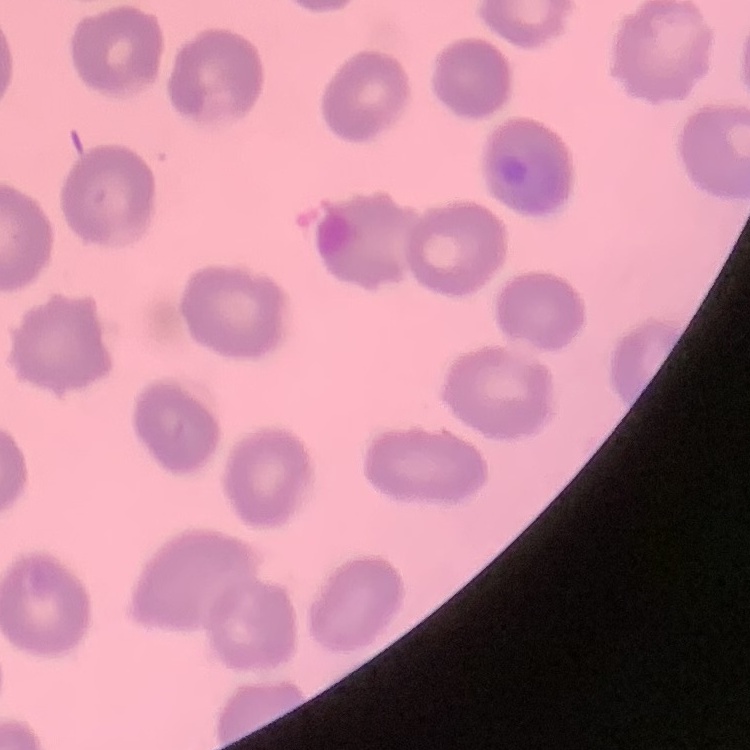
red_blood_cell_morphology: no rouleaux formation
stain: Field's or Giemsa
preparation: thin blood smear
image_type: square crop of a larger photomicrograph